Assess the morphology of the red blood cells.
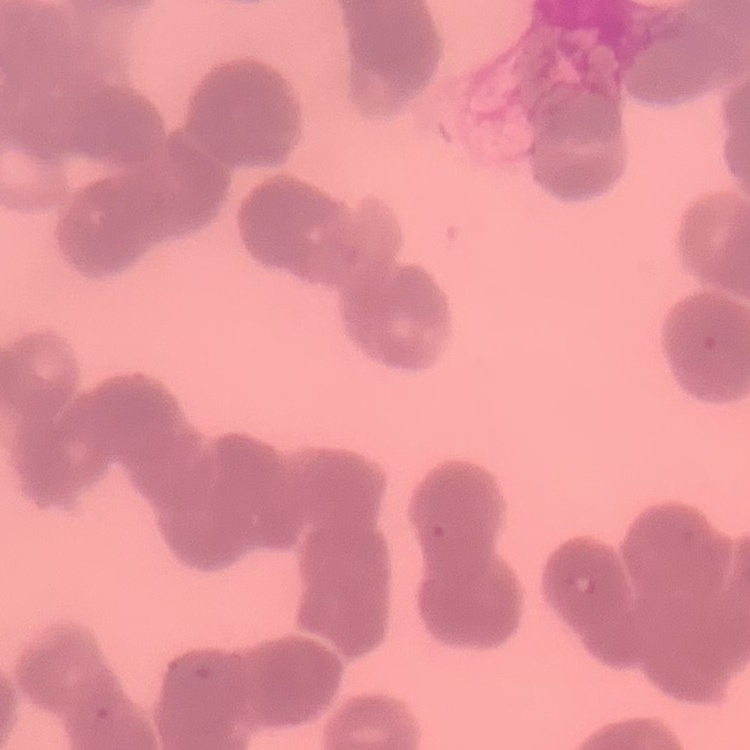
They show rouleaux formation.

Thin blood smear. Field's or Giemsa stain. One tile cut from a larger photomicrograph.